Name the blood parasite species.
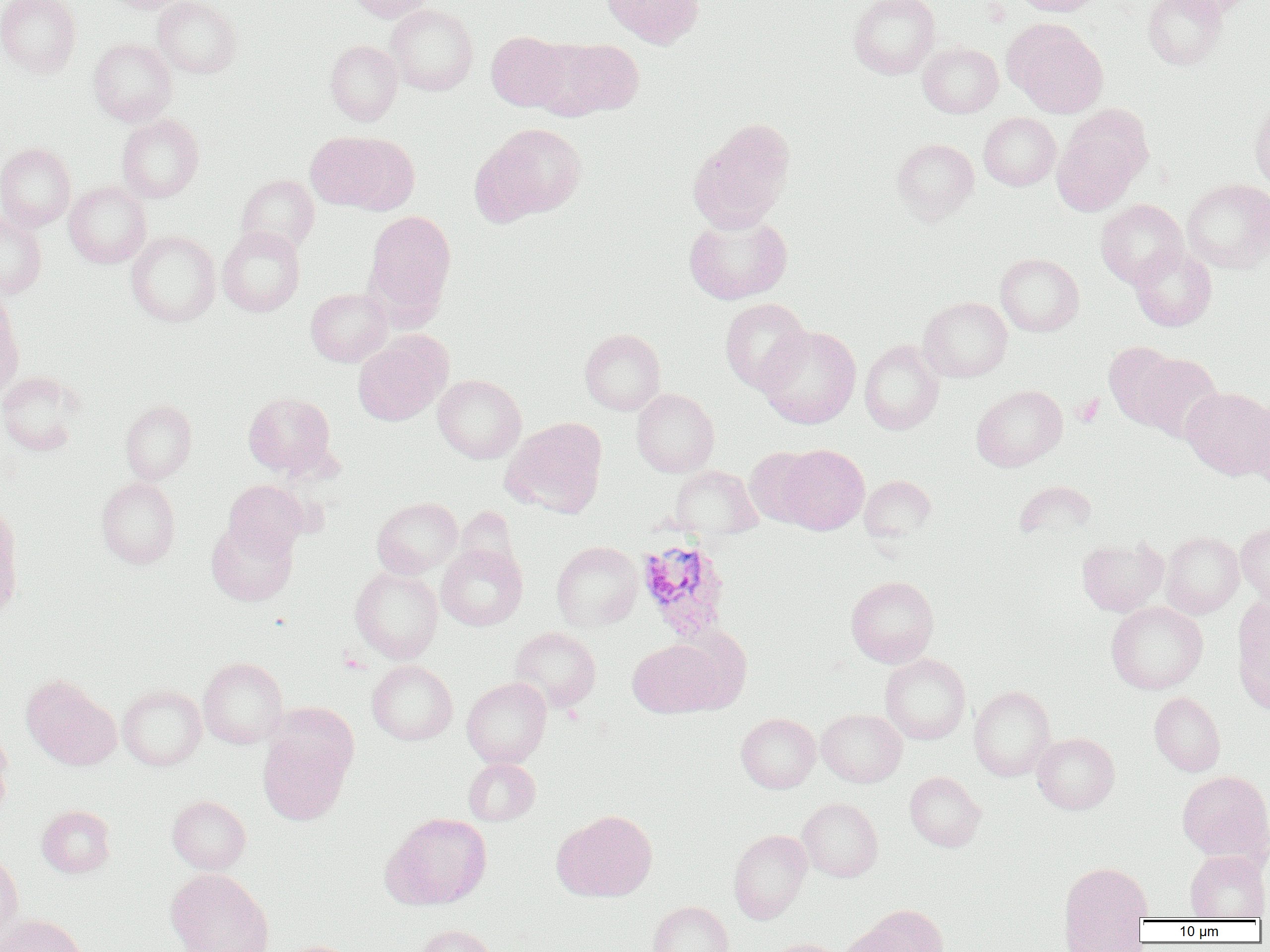

Plasmodium ovale.

Approximate bounding boxes as (x1, y1, x2, y2) in pixels. Platelet locations: (1072, 394, 1104, 427). Plasmodium ovale-infected red blood cell locations: (636, 538, 731, 641). Uninfected red blood cell locations: (0, 0, 80, 79), (105, 0, 186, 13), (153, 0, 242, 78), (347, 0, 434, 22), (601, 0, 703, 48), (849, 0, 940, 79), (1012, 0, 1104, 16), (1143, 0, 1227, 70), (1167, 0, 1255, 18), (386, 4, 477, 96), (1004, 19, 1108, 118), (487, 31, 571, 111), (539, 38, 644, 118), (89, 39, 176, 126), (325, 40, 403, 126), (918, 42, 1003, 117), (1249, 96, 1270, 192), (979, 112, 1061, 191), (1051, 112, 1149, 215), (117, 115, 204, 202), (688, 118, 795, 232), (479, 122, 588, 220), (307, 131, 415, 214), (892, 138, 979, 222), (0, 143, 75, 231), (237, 175, 319, 253), (1182, 179, 1270, 272), (64, 182, 151, 268), (1095, 199, 1188, 287), (364, 210, 456, 320), (0, 211, 46, 298), (683, 213, 792, 304), (217, 226, 305, 316), (126, 231, 220, 327), (1129, 245, 1216, 331), (995, 253, 1084, 336), (306, 288, 392, 366), (0, 295, 22, 399), (919, 297, 1012, 382), (719, 298, 811, 394), (757, 325, 861, 428), (579, 329, 666, 415), (353, 335, 448, 426), (859, 339, 944, 435), (1104, 341, 1185, 429), (1136, 353, 1223, 443), (0, 372, 82, 455), (433, 374, 526, 463), (972, 385, 1067, 471), (1181, 387, 1270, 479), (632, 388, 719, 477), (243, 392, 335, 475), (1245, 398, 1269, 489), (120, 399, 197, 483), (502, 418, 607, 518), (777, 444, 869, 534), (746, 447, 821, 528), (669, 465, 763, 542), (859, 475, 936, 543), (97, 477, 180, 568), (224, 480, 308, 559), (1014, 480, 1097, 540), (372, 497, 462, 578), (0, 506, 22, 618), (455, 506, 519, 578), (206, 519, 297, 606), (1236, 521, 1270, 604), (1161, 531, 1244, 618), (1077, 537, 1168, 616), (551, 541, 642, 631), (436, 544, 527, 630), (350, 567, 442, 663), (846, 576, 939, 667), (1232, 595, 1270, 711), (1106, 602, 1207, 693), (509, 627, 601, 712), (628, 638, 725, 717), (880, 654, 970, 744), (198, 657, 287, 748), (367, 660, 457, 745), (21, 675, 121, 770), (462, 677, 551, 768), (118, 685, 205, 770), (969, 686, 1055, 781), (1149, 692, 1225, 776), (817, 709, 906, 787), (736, 713, 820, 793), (0, 728, 13, 819), (257, 731, 351, 825), (1032, 733, 1119, 814), (464, 758, 540, 825), (1177, 770, 1269, 864), (905, 771, 985, 851), (167, 796, 250, 873), (797, 798, 883, 882), (36, 805, 115, 877), (554, 809, 657, 901), (383, 813, 492, 909), (729, 830, 812, 923), (1185, 850, 1269, 920), (0, 851, 23, 946), (1059, 861, 1153, 934), (166, 868, 272, 952), (647, 901, 733, 952), (849, 904, 948, 952), (1, 914, 88, 952), (1061, 914, 1150, 951), (414, 924, 495, 952), (765, 938, 846, 952), (276, 940, 358, 952). Optical microscopy. Captured at 1000x magnification. Image is 1270×952 pixels. Thin blood film. One field of a larger specimen.